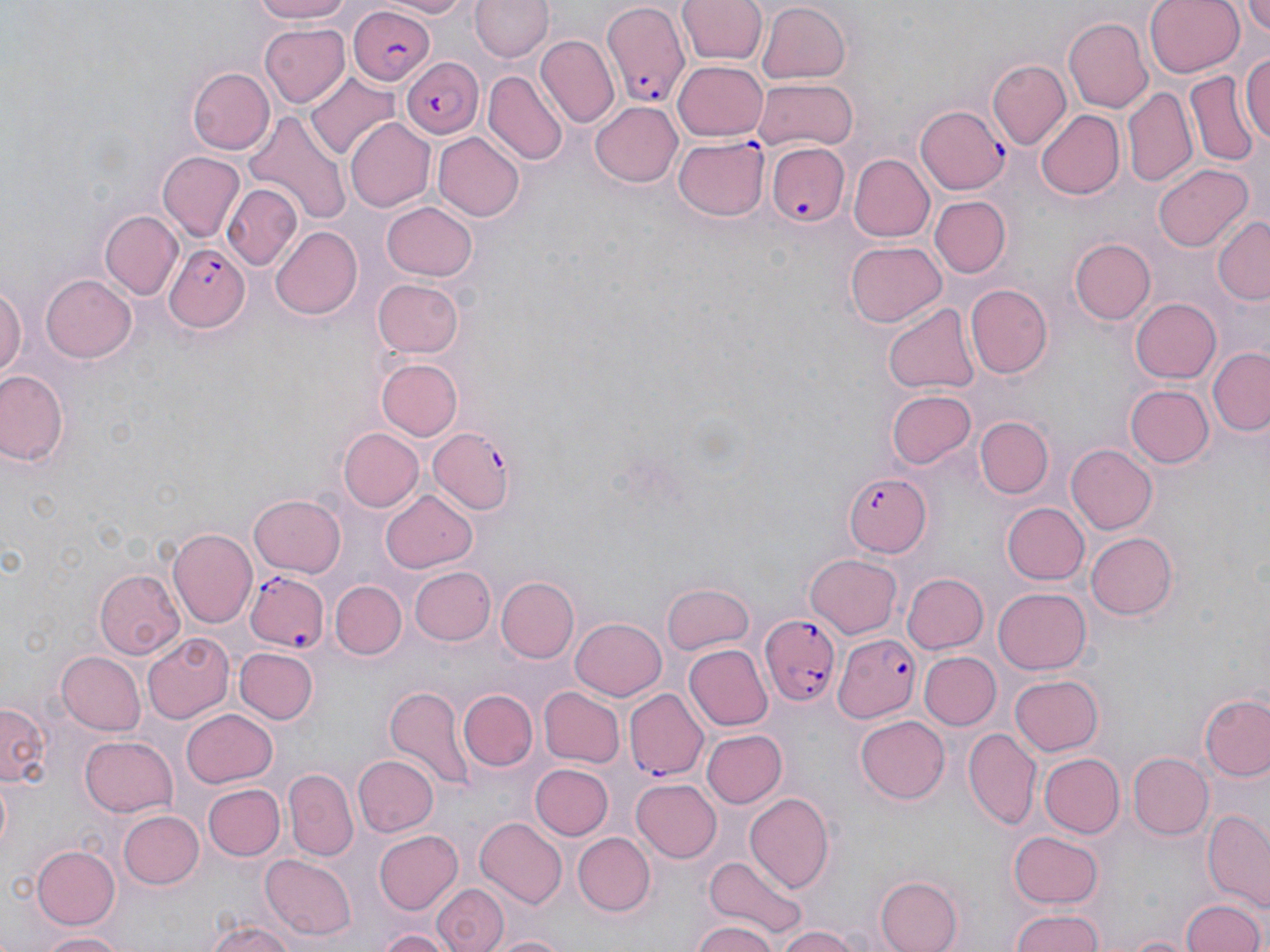
Approximate bounding boxes as (x1, y1, x2, y2) in pixels. Uninfected red blood cell locations: (248, 0, 354, 24), (378, 0, 474, 18), (676, 0, 768, 66), (1145, 0, 1246, 76), (472, 1, 551, 64), (1240, 1, 1270, 37), (755, 3, 851, 86), (1063, 16, 1153, 113), (258, 25, 353, 107), (535, 36, 619, 129), (1242, 47, 1270, 148), (1220, 56, 1266, 159), (987, 59, 1070, 151), (674, 60, 770, 141), (187, 67, 273, 155), (485, 72, 568, 166), (1186, 73, 1262, 166), (306, 74, 401, 162), (752, 78, 860, 153), (1124, 86, 1197, 190), (1053, 95, 1200, 196), (591, 101, 683, 186), (1036, 108, 1128, 201), (242, 112, 349, 230), (344, 118, 435, 211), (433, 132, 523, 221), (156, 152, 244, 242), (851, 153, 936, 242), (1154, 163, 1251, 250), (222, 184, 302, 270), (931, 195, 1013, 278), (382, 200, 479, 281), (101, 210, 182, 297), (1211, 216, 1270, 307), (271, 227, 363, 321), (1072, 239, 1156, 324), (845, 241, 945, 327), (40, 271, 137, 362), (0, 279, 25, 382), (373, 279, 463, 358), (965, 282, 1052, 376), (1132, 296, 1224, 383), (883, 303, 979, 396), (1209, 345, 1270, 437), (375, 358, 462, 441), (1, 369, 67, 467), (1125, 383, 1212, 466), (887, 389, 975, 470), (975, 414, 1052, 498), (340, 427, 425, 512), (1067, 445, 1157, 534), (380, 487, 477, 572), (249, 494, 345, 578), (1002, 502, 1089, 585), (168, 528, 258, 629), (1086, 532, 1180, 619), (804, 553, 901, 636), (407, 566, 494, 646), (94, 568, 183, 660), (900, 573, 989, 656), (497, 577, 579, 663), (331, 580, 407, 660), (660, 584, 753, 657), (992, 587, 1091, 674), (569, 616, 666, 701), (141, 634, 235, 723), (683, 644, 772, 731), (235, 648, 318, 726), (56, 651, 145, 734), (918, 651, 1000, 730), (1009, 675, 1102, 756), (385, 685, 472, 791), (537, 686, 624, 767), (459, 690, 538, 772), (1200, 693, 1270, 782), (1, 700, 51, 789), (183, 708, 278, 787), (854, 715, 950, 805), (963, 727, 1039, 829), (698, 730, 787, 809), (80, 735, 178, 817), (1040, 752, 1124, 838), (1128, 752, 1212, 838), (353, 757, 438, 837), (529, 764, 613, 838), (285, 767, 357, 860), (630, 779, 721, 863), (202, 783, 284, 862), (745, 794, 833, 892), (120, 809, 205, 889), (1201, 810, 1269, 906), (474, 817, 568, 909), (373, 829, 463, 915), (1008, 830, 1103, 910), (572, 832, 653, 916), (31, 844, 121, 929), (261, 855, 355, 940), (705, 858, 803, 938), (874, 873, 962, 952), (433, 884, 508, 952), (1181, 897, 1264, 952), (1006, 910, 1109, 952), (204, 919, 297, 952), (693, 919, 778, 952), (775, 925, 859, 952), (374, 928, 450, 952), (39, 930, 129, 951), (487, 932, 573, 952), (1120, 933, 1195, 952). Plasmodium falciparum-infected red blood cell locations: (598, 3, 689, 108), (345, 6, 435, 86), (399, 58, 483, 141), (916, 104, 1009, 193), (674, 136, 767, 221), (765, 142, 847, 227), (165, 243, 249, 332), (425, 426, 516, 518), (843, 471, 932, 556), (244, 571, 328, 651), (759, 613, 840, 710), (834, 632, 921, 722), (625, 688, 710, 779). Slide-level diagnosis: Plasmodium falciparum. Thin blood film. Optical microscopy. Image is 1270×952 pixels. May-Grünwald-Giemsa-stained preparation. One field of a larger specimen. Captured at 1000x magnification.